Identify the parasite.
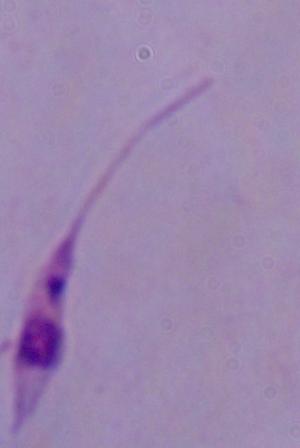
This is Leishmania.

Summary:
  - Magnification: 1000x
  - Modality: photomicrograph